Identify the blood parasite species.
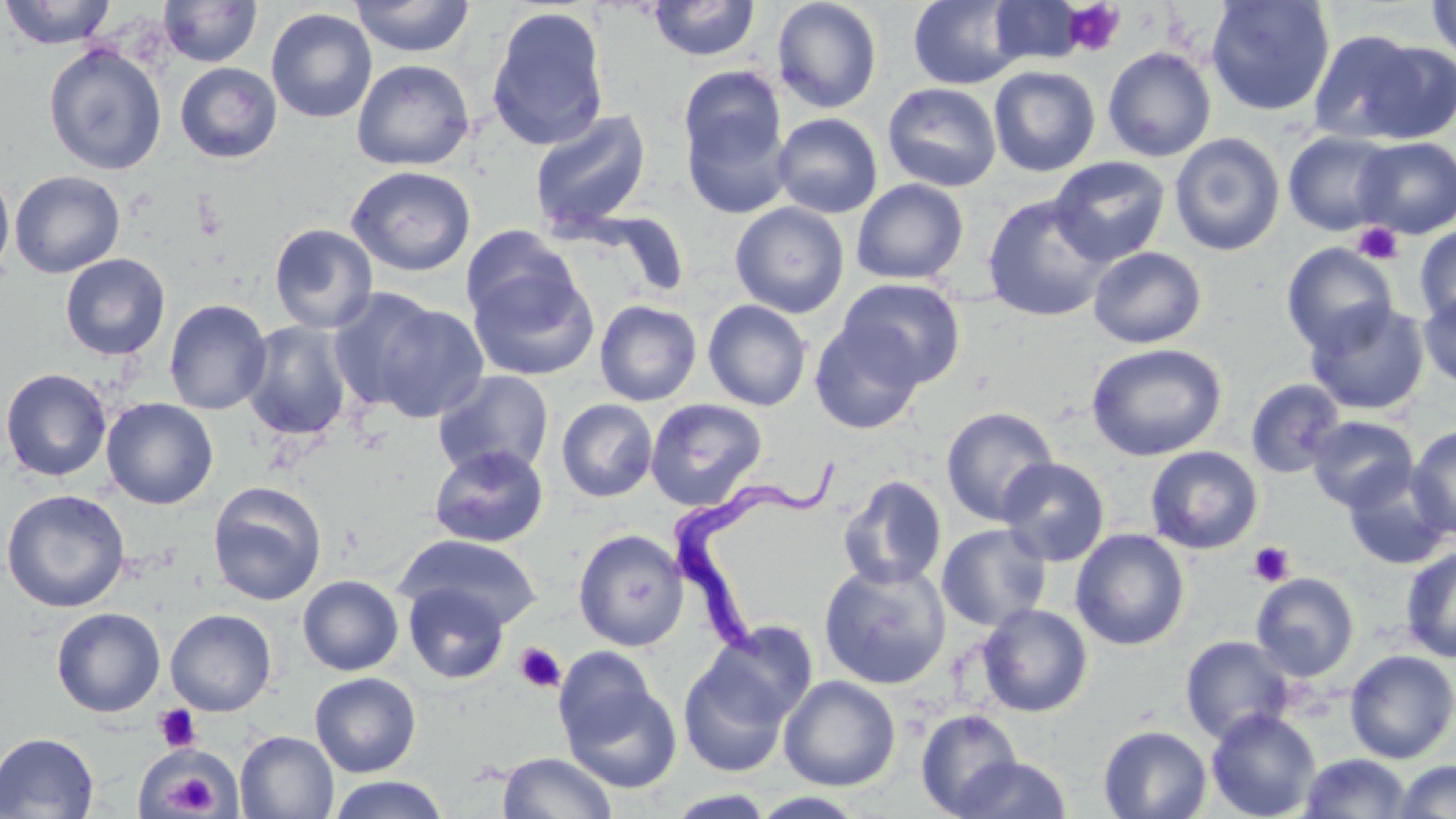

Trypanosoma brucei.

platelet_locations: 'approximate bounding boxes as (x1,y1)-(x2,y2) corner pairs in pixels: (1063,1)-(1125,56), (1352,222)-(1403,266), (1248,541)-(1295,587), (514,642)-(567,694), (155,705)-(201,752), (164,768)-(221,816)'
uninfected_red_blood_cell_locations: 'approximate bounding boxes as (x1,y1)-(x2,y2) corner pairs in pixels: (0,0)-(118,50), (158,0)-(262,68), (349,0)-(475,58), (648,0)-(760,61), (771,0)-(882,114), (908,0)-(1028,90), (1206,0)-(1335,117), (1426,0)-(1456,66), (989,1)-(1086,65), (486,5)-(610,151), (266,8)-(377,123), (1309,29)-(1442,143), (43,42)-(167,176), (1102,47)-(1217,162), (351,59)-(475,171), (175,62)-(282,164), (678,66)-(787,181), (988,66)-(1101,177), (882,82)-(1002,192), (682,106)-(794,220), (529,109)-(652,235), (772,113)-(883,218), (1283,130)-(1398,236), (1169,133)-(1285,256), (1354,137)-(1456,238), (1048,156)-(1171,267), (0,165)-(15,285), (346,165)-(476,277), (9,170)-(125,277), (850,179)-(969,285), (982,194)-(1114,322), (730,202)-(850,318), (269,223)-(378,334), (1415,224)-(1456,326), (461,225)-(578,332), (1281,242)-(1398,355), (1088,246)-(1206,348), (60,253)-(170,361), (467,262)-(598,380), (837,277)-(967,390), (328,289)-(447,413), (1418,290)-(1456,389), (163,299)-(273,415), (702,299)-(812,411), (365,300)-(490,424), (594,300)-(703,406), (1304,300)-(1428,416), (810,320)-(925,435), (241,321)-(353,442), (1086,343)-(1228,461), (0,368)-(113,482), (433,370)-(554,479), (1245,378)-(1345,478), (101,398)-(218,509), (556,398)-(658,503), (646,398)-(767,511), (941,406)-(1059,526), (1306,415)-(1418,513), (1407,426)-(1456,540), (428,444)-(548,548), (1145,446)-(1263,554), (997,457)-(1110,566), (1343,468)-(1452,570), (838,475)-(948,590), (207,481)-(327,605), (1,488)-(131,613), (936,523)-(1052,632), (573,528)-(689,651), (1070,528)-(1190,651), (397,535)-(542,632), (1400,546)-(1456,663), (818,561)-(952,690), (1250,572)-(1360,681), (298,574)-(404,676), (403,580)-(509,684), (976,603)-(1093,717), (51,607)-(166,717), (165,609)-(277,716), (701,620)-(819,730), (1180,635)-(1296,744), (678,649)-(796,778), (1344,650)-(1456,763), (560,671)-(681,793), (309,672)-(421,777), (778,675)-(901,791), (1205,708)-(1321,819), (915,709)-(1024,817), (1098,725)-(1212,819), (235,730)-(339,819), (0,732)-(99,818), (136,744)-(234,818), (498,752)-(617,819), (1298,753)-(1412,818), (950,754)-(1073,818), (1393,759)-(1456,818), (327,775)-(449,818), (665,789)-(778,818), (750,791)-(869,818)'
preparation: thin blood smear
field_of_view: single
stain: May-Grünwald-Giemsa
modality: optical microscopy
trypanosoma_brucei_locations: 'approximate bounding boxes as (x1,y1)-(x2,y2) corner pairs in pixels: (672,455)-(845,662)'
image_size: 1456×819 pixels
magnification: 1000x